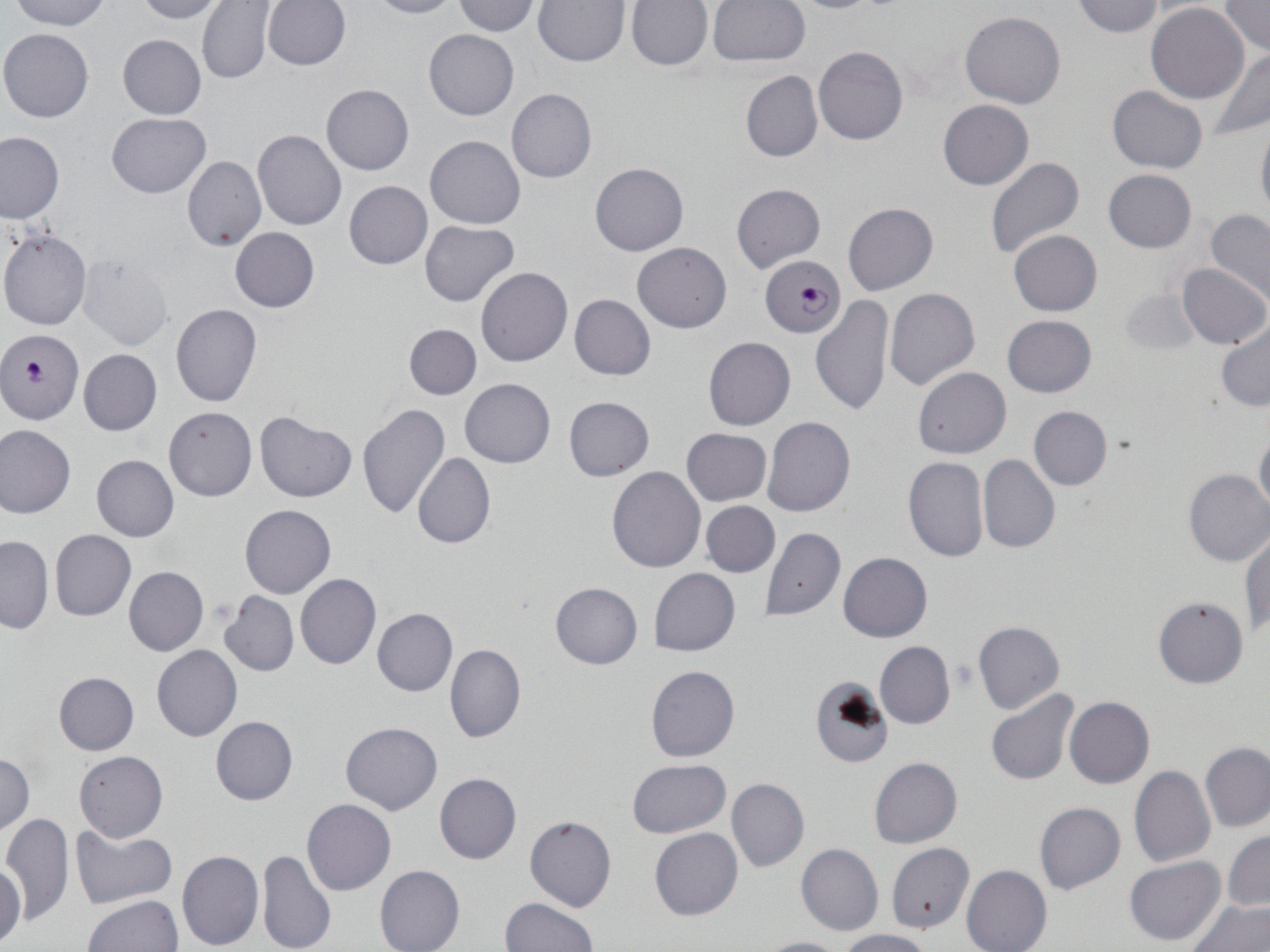
slide-level diagnosis = Plasmodium falciparum
image size = 1270×952 pixels
Plasmodium falciparum-infected red blood cell locations = approximate bounding boxes as named x1/y1/x2/y2 corners in pixels: (x1=759, y1=256, x2=845, y2=337), (x1=1, y1=330, x2=84, y2=425)
uninfected red blood cell locations = approximate bounding boxes as named x1/y1/x2/y2 corners in pixels: (x1=11, y1=0, x2=110, y2=30), (x1=136, y1=0, x2=224, y2=23), (x1=197, y1=0, x2=275, y2=84), (x1=369, y1=0, x2=461, y2=19), (x1=533, y1=0, x2=630, y2=67), (x1=1070, y1=0, x2=1165, y2=38), (x1=262, y1=1, x2=351, y2=70), (x1=452, y1=1, x2=541, y2=36), (x1=627, y1=1, x2=712, y2=70), (x1=707, y1=1, x2=809, y2=67), (x1=781, y1=1, x2=887, y2=14), (x1=1219, y1=1, x2=1270, y2=57), (x1=1147, y1=3, x2=1249, y2=102), (x1=959, y1=11, x2=1065, y2=108), (x1=0, y1=28, x2=94, y2=122), (x1=424, y1=29, x2=519, y2=120), (x1=118, y1=34, x2=206, y2=118), (x1=814, y1=46, x2=908, y2=146), (x1=1209, y1=48, x2=1270, y2=138), (x1=741, y1=71, x2=822, y2=162), (x1=321, y1=84, x2=414, y2=175), (x1=1107, y1=85, x2=1208, y2=172), (x1=507, y1=88, x2=597, y2=182), (x1=939, y1=99, x2=1033, y2=189), (x1=107, y1=113, x2=209, y2=198), (x1=1256, y1=119, x2=1270, y2=224), (x1=253, y1=129, x2=346, y2=230), (x1=0, y1=132, x2=64, y2=223), (x1=425, y1=135, x2=524, y2=228), (x1=182, y1=155, x2=266, y2=250), (x1=984, y1=157, x2=1084, y2=259), (x1=590, y1=162, x2=687, y2=256), (x1=1103, y1=169, x2=1196, y2=252), (x1=345, y1=181, x2=432, y2=269), (x1=731, y1=183, x2=826, y2=274), (x1=844, y1=203, x2=938, y2=295), (x1=1204, y1=209, x2=1270, y2=308), (x1=419, y1=221, x2=519, y2=306), (x1=230, y1=227, x2=318, y2=313), (x1=0, y1=230, x2=91, y2=331), (x1=1008, y1=230, x2=1102, y2=315), (x1=633, y1=241, x2=731, y2=332), (x1=77, y1=254, x2=173, y2=352), (x1=1178, y1=263, x2=1269, y2=348), (x1=476, y1=267, x2=572, y2=366), (x1=1119, y1=287, x2=1200, y2=357), (x1=885, y1=288, x2=979, y2=389), (x1=570, y1=294, x2=655, y2=380), (x1=811, y1=294, x2=894, y2=416), (x1=171, y1=304, x2=262, y2=407), (x1=1003, y1=315, x2=1097, y2=397), (x1=1216, y1=320, x2=1270, y2=411), (x1=405, y1=324, x2=480, y2=399), (x1=703, y1=336, x2=795, y2=430), (x1=79, y1=349, x2=162, y2=436), (x1=913, y1=367, x2=1010, y2=457), (x1=460, y1=378, x2=554, y2=467), (x1=564, y1=396, x2=654, y2=479), (x1=357, y1=403, x2=450, y2=521), (x1=163, y1=406, x2=256, y2=502), (x1=1028, y1=406, x2=1112, y2=491), (x1=254, y1=413, x2=356, y2=503), (x1=763, y1=417, x2=855, y2=516), (x1=0, y1=425, x2=76, y2=517), (x1=680, y1=428, x2=772, y2=506), (x1=1255, y1=431, x2=1270, y2=515), (x1=413, y1=453, x2=495, y2=549), (x1=978, y1=453, x2=1060, y2=554), (x1=92, y1=454, x2=179, y2=540), (x1=903, y1=456, x2=988, y2=562), (x1=606, y1=467, x2=706, y2=572), (x1=1182, y1=469, x2=1270, y2=567), (x1=701, y1=501, x2=780, y2=577), (x1=240, y1=504, x2=336, y2=598), (x1=759, y1=526, x2=845, y2=621), (x1=50, y1=529, x2=135, y2=621), (x1=1241, y1=531, x2=1270, y2=640), (x1=0, y1=535, x2=54, y2=634), (x1=759, y1=535, x2=928, y2=629), (x1=838, y1=552, x2=931, y2=642), (x1=123, y1=565, x2=208, y2=655), (x1=649, y1=567, x2=740, y2=656), (x1=295, y1=574, x2=380, y2=670), (x1=549, y1=581, x2=643, y2=669), (x1=220, y1=592, x2=299, y2=676), (x1=1152, y1=596, x2=1248, y2=687), (x1=372, y1=608, x2=457, y2=696), (x1=973, y1=621, x2=1064, y2=714), (x1=875, y1=641, x2=954, y2=729), (x1=445, y1=643, x2=525, y2=742), (x1=152, y1=645, x2=242, y2=742), (x1=645, y1=664, x2=740, y2=762), (x1=53, y1=671, x2=139, y2=755), (x1=809, y1=677, x2=892, y2=769), (x1=986, y1=689, x2=1080, y2=786), (x1=1065, y1=696, x2=1153, y2=788), (x1=210, y1=716, x2=298, y2=804), (x1=340, y1=721, x2=442, y2=814), (x1=1199, y1=743, x2=1269, y2=832), (x1=74, y1=750, x2=169, y2=842), (x1=0, y1=753, x2=35, y2=838), (x1=869, y1=758, x2=962, y2=848), (x1=626, y1=759, x2=730, y2=838), (x1=1128, y1=764, x2=1215, y2=866), (x1=435, y1=773, x2=521, y2=864), (x1=727, y1=778, x2=809, y2=872), (x1=302, y1=799, x2=396, y2=895), (x1=1034, y1=802, x2=1125, y2=894), (x1=1, y1=813, x2=74, y2=925), (x1=524, y1=815, x2=616, y2=912), (x1=69, y1=825, x2=176, y2=910), (x1=650, y1=828, x2=742, y2=920), (x1=1223, y1=830, x2=1270, y2=911), (x1=796, y1=844, x2=884, y2=935), (x1=886, y1=844, x2=973, y2=932), (x1=256, y1=848, x2=337, y2=952), (x1=176, y1=850, x2=263, y2=950), (x1=1123, y1=856, x2=1225, y2=946), (x1=0, y1=863, x2=26, y2=946), (x1=962, y1=864, x2=1051, y2=952), (x1=376, y1=865, x2=464, y2=952), (x1=82, y1=895, x2=183, y2=952), (x1=501, y1=897, x2=597, y2=951), (x1=1189, y1=899, x2=1270, y2=952), (x1=836, y1=929, x2=933, y2=952), (x1=755, y1=937, x2=847, y2=952)
modality = optical microscopy
magnification = 1000x
field of view = one of a larger specimen
stain = May-Grünwald-Giemsa
preparation = thin blood film